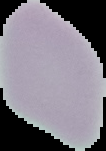
From a thin blood film. Result: no Plasmodium parasites seen. Segmented cell region on a black background. Image is 106×151 pixels.